Report the malaria status of this cell.
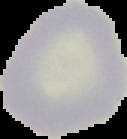
It is uninfected.

From a thin blood smear. The area outside the segmented cell region is set to black. Image is 127×139 pixels.